Locate malaria parasites and leukocytes.
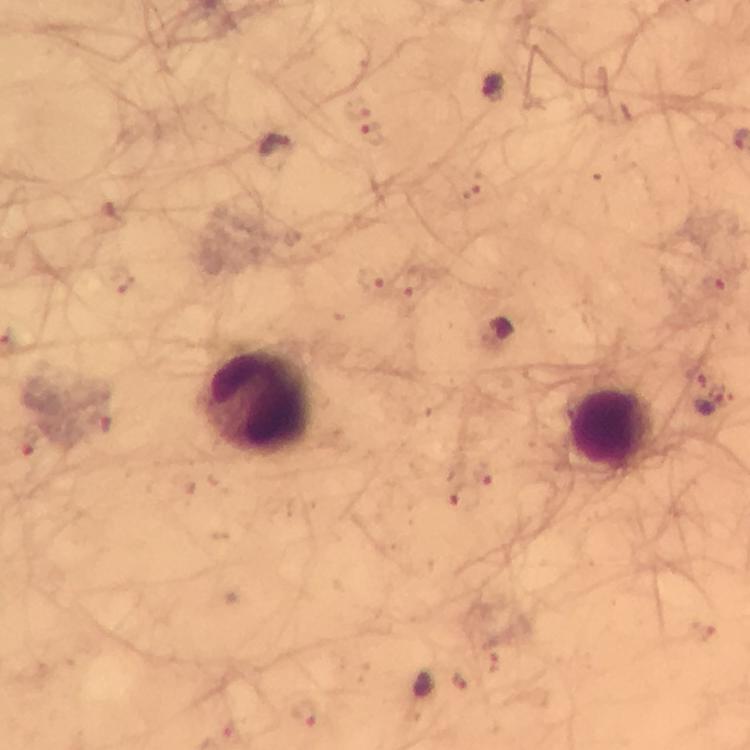
Approximate centers as {x, y} in pixels.
Malaria parasites: {492, 85}, {374, 129}, {277, 149}, {710, 393}.
Leukocytes: {258, 403}, {613, 429}.

Summary:
  - Immersion oil: applied
  - Image size: 750×750 pixels
  - Capture: smartphone photograph through a microscope
  - Preparation: thick smear
  - Stain: Giemsa
  - Magnification: 100x
  - Cropped from: a single field of view
  - Context: from a diagnostic examination for malaria